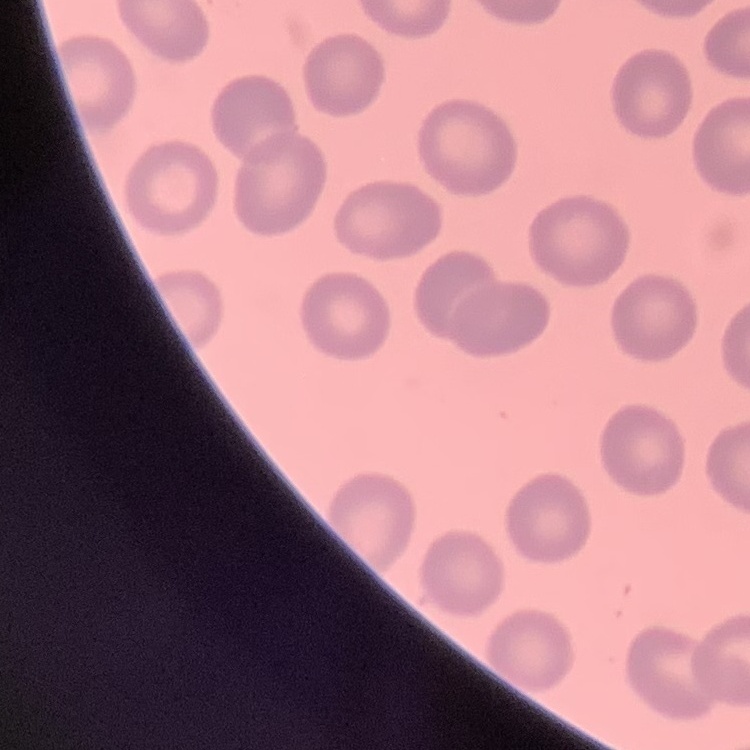
erythrocyte morphology = no rouleaux formation
image type = one tile cut from a larger photomicrograph
stain = Field's or Giemsa
preparation = thin peripheral smear